State which parasite is depicted.
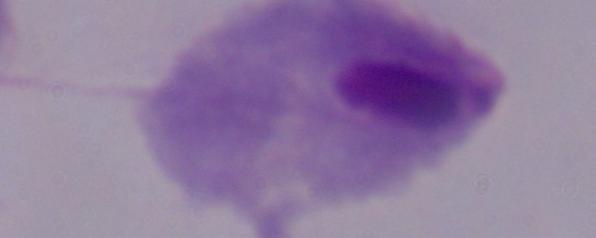

A trichomonad.

1000x magnification. Micrograph.